Report the malaria status of this cell.
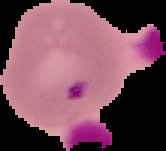
It is parasitized.

Summary:
  - Image size: 166×151 pixels
  - Image type: segmented cell region with the area outside set to black
  - Preparation: thin blood film